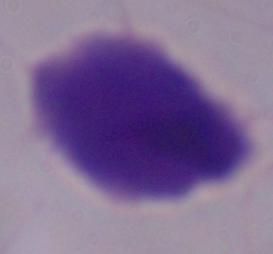

modality = micrograph
magnification = 1000x
identification = trichomonad